Assess this cell for malaria.
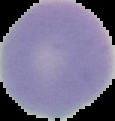

It is uninfected.

preparation = thin blood smear
image type = segmented cell region with the area outside set to black
image size = 115×121 pixels